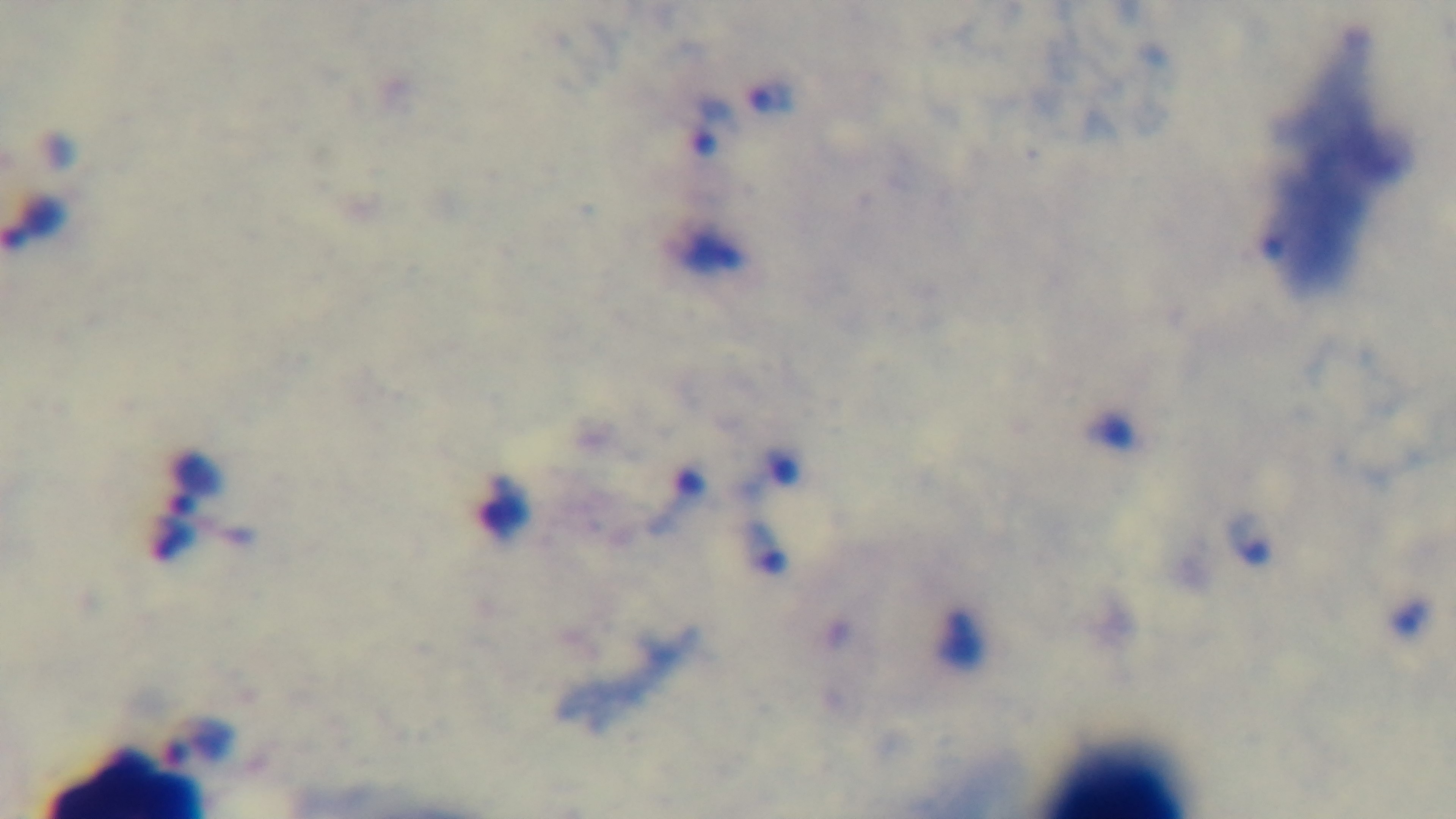

{
  "preparation": "thick blood film",
  "stain": "Giemsa",
  "objective": "100x oil immersion",
  "capture": "mounted 4K digital camera",
  "field_of_view": "single",
  "malaria_status": "infected",
  "modality": "light microscopy"
}